Outline every leukocyte.
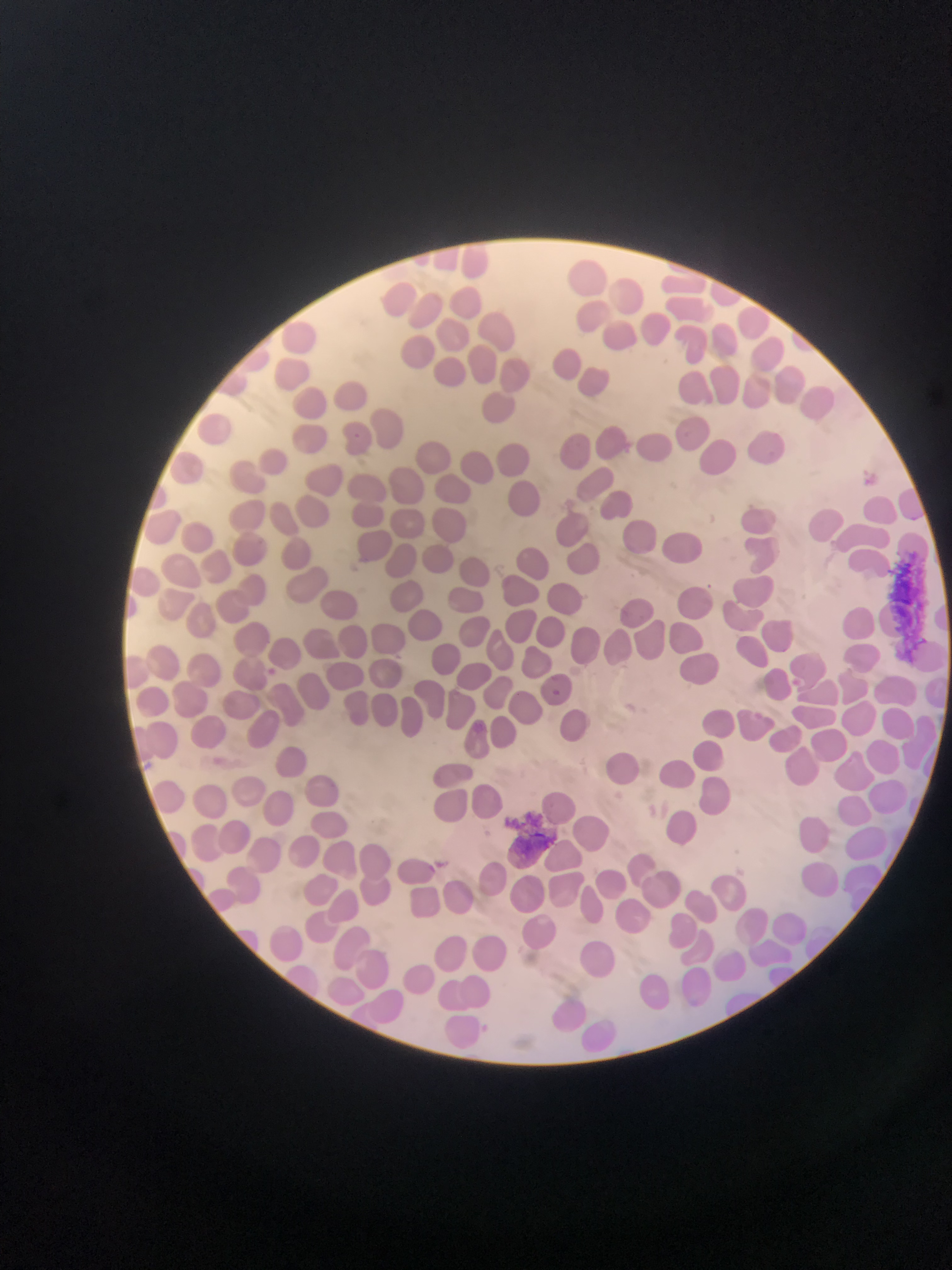
No leukocytes observed.

Approximate bounding boxes as (left, top, right, bottom) in pixels. Artifact (stain precipitate or debris) locations: (894, 554, 927, 665), (504, 809, 565, 854). Malaria parasite locations: (353, 429, 367, 442), (623, 439, 631, 460), (865, 473, 877, 488), (707, 579, 720, 591), (267, 668, 286, 689), (553, 685, 565, 700), (475, 719, 490, 733), (436, 857, 446, 867), (424, 864, 437, 874), (481, 1018, 490, 1035). One field of view. Collected in Ghana. Thin blood film. Mobile-phone photograph taken through the microscope. Image is 952×1270 pixels.